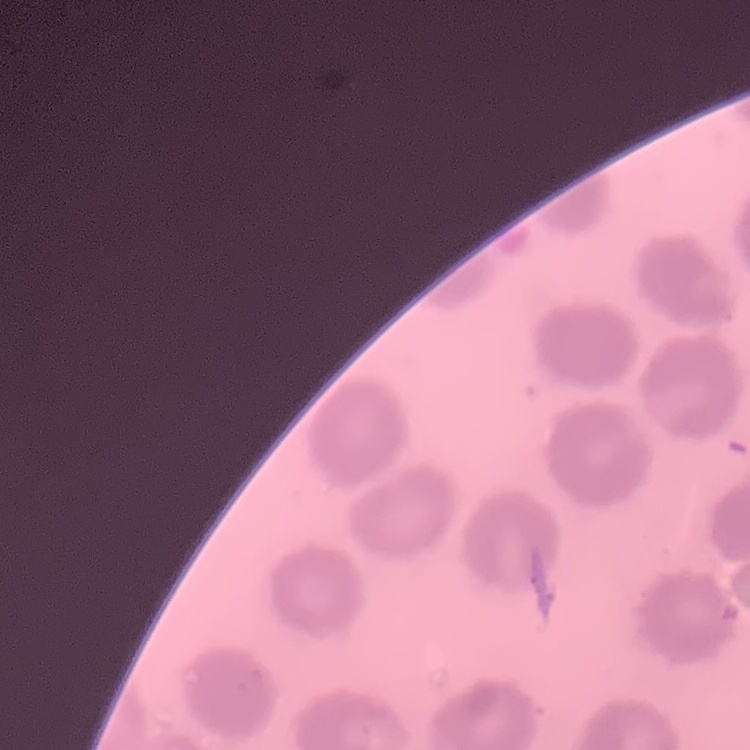

The erythrocytes exhibit no rouleaux formation. Thin blood smear. Stained with either Field's or Giemsa. Square crop of a larger photomicrograph.